Locate platelets.
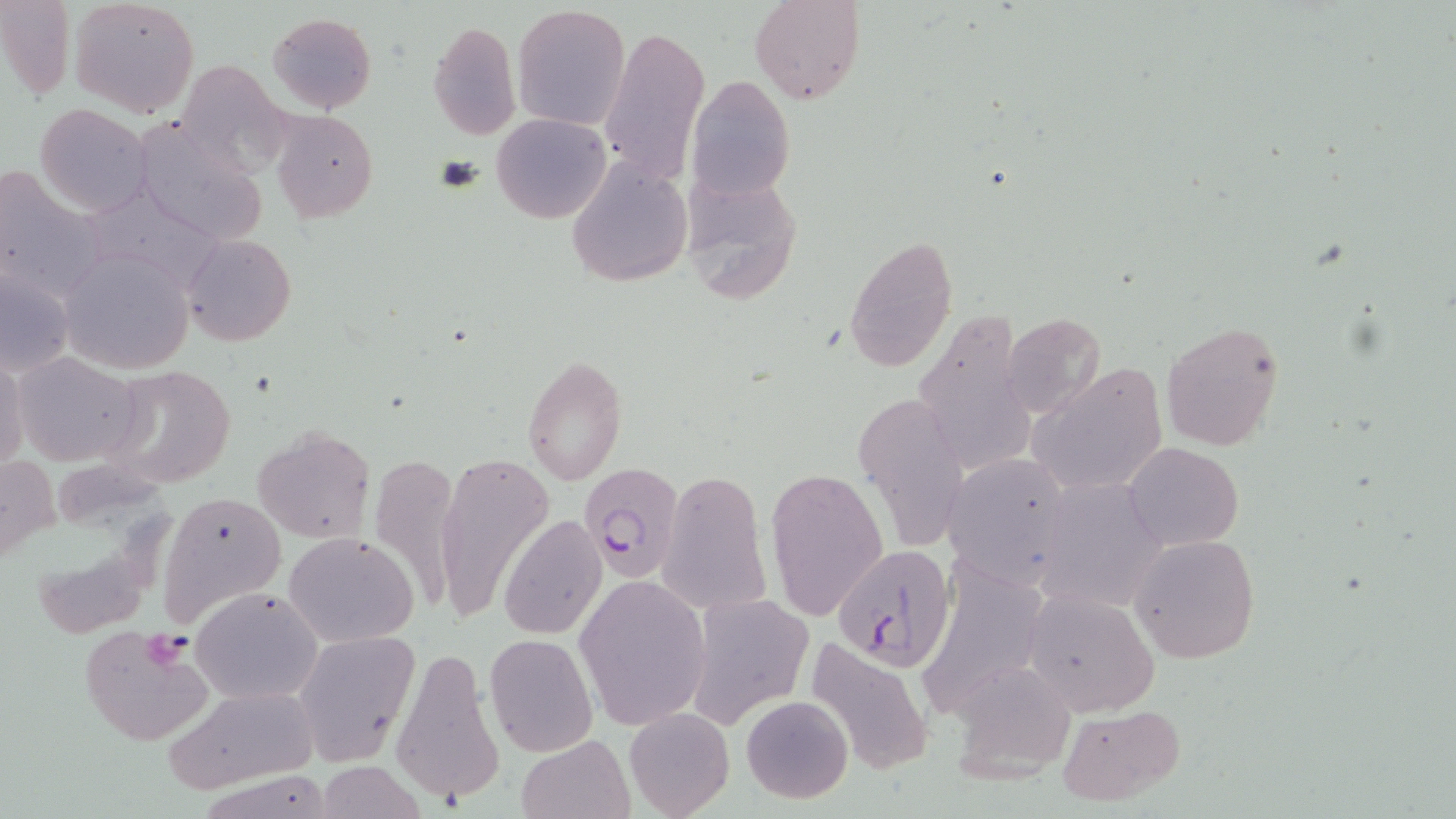

Approximate bounding boxes as (x1, y1, x2, y2) in pixels.
Platelets: (432, 153, 484, 193), (142, 633, 194, 671).

Summary:
  - Uninfected red blood cell locations: (0, 0, 75, 99), (68, 0, 199, 117), (751, 0, 865, 104), (513, 4, 631, 130), (266, 11, 377, 113), (428, 19, 520, 139), (597, 23, 710, 188), (170, 60, 293, 177), (686, 74, 795, 202), (35, 103, 152, 216), (270, 109, 378, 223), (491, 112, 611, 224), (132, 117, 266, 243), (565, 155, 692, 288), (0, 165, 99, 298), (677, 169, 804, 305), (84, 185, 224, 295), (182, 233, 297, 347), (845, 234, 957, 373), (58, 244, 197, 375), (1, 267, 75, 378), (1001, 312, 1106, 419), (913, 317, 1037, 484), (1162, 321, 1286, 452), (12, 351, 144, 466), (521, 355, 628, 484), (0, 357, 26, 472), (101, 363, 236, 489), (1029, 364, 1170, 497), (853, 393, 972, 554), (252, 425, 376, 543), (1123, 441, 1243, 550), (365, 451, 463, 614), (942, 451, 1072, 588), (1, 452, 61, 563), (433, 452, 553, 622), (767, 467, 889, 622), (659, 468, 773, 619), (1036, 480, 1169, 612), (159, 490, 286, 622), (499, 514, 607, 640), (284, 532, 420, 645), (1129, 535, 1260, 663), (925, 566, 1050, 708), (574, 575, 709, 729), (191, 585, 324, 706), (1022, 589, 1160, 717), (686, 593, 813, 728), (78, 626, 216, 747), (292, 629, 420, 766), (485, 634, 597, 756), (800, 635, 936, 777), (390, 644, 505, 811), (947, 662, 1077, 784), (159, 685, 322, 794), (740, 695, 853, 804), (1053, 702, 1186, 807), (625, 709, 733, 819), (516, 735, 633, 819), (315, 761, 425, 818)
  - Plasmodium falciparum-infected red blood cell locations: (577, 463, 685, 585), (831, 543, 957, 670)
  - Slide-level diagnosis: Plasmodium falciparum
  - Magnification: 1000x
  - Modality: optical microscopy
  - Stain: May-Grünwald-Giemsa
  - Field of view: one of a larger specimen
  - Preparation: thin blood film
  - Image size: 1456×819 pixels